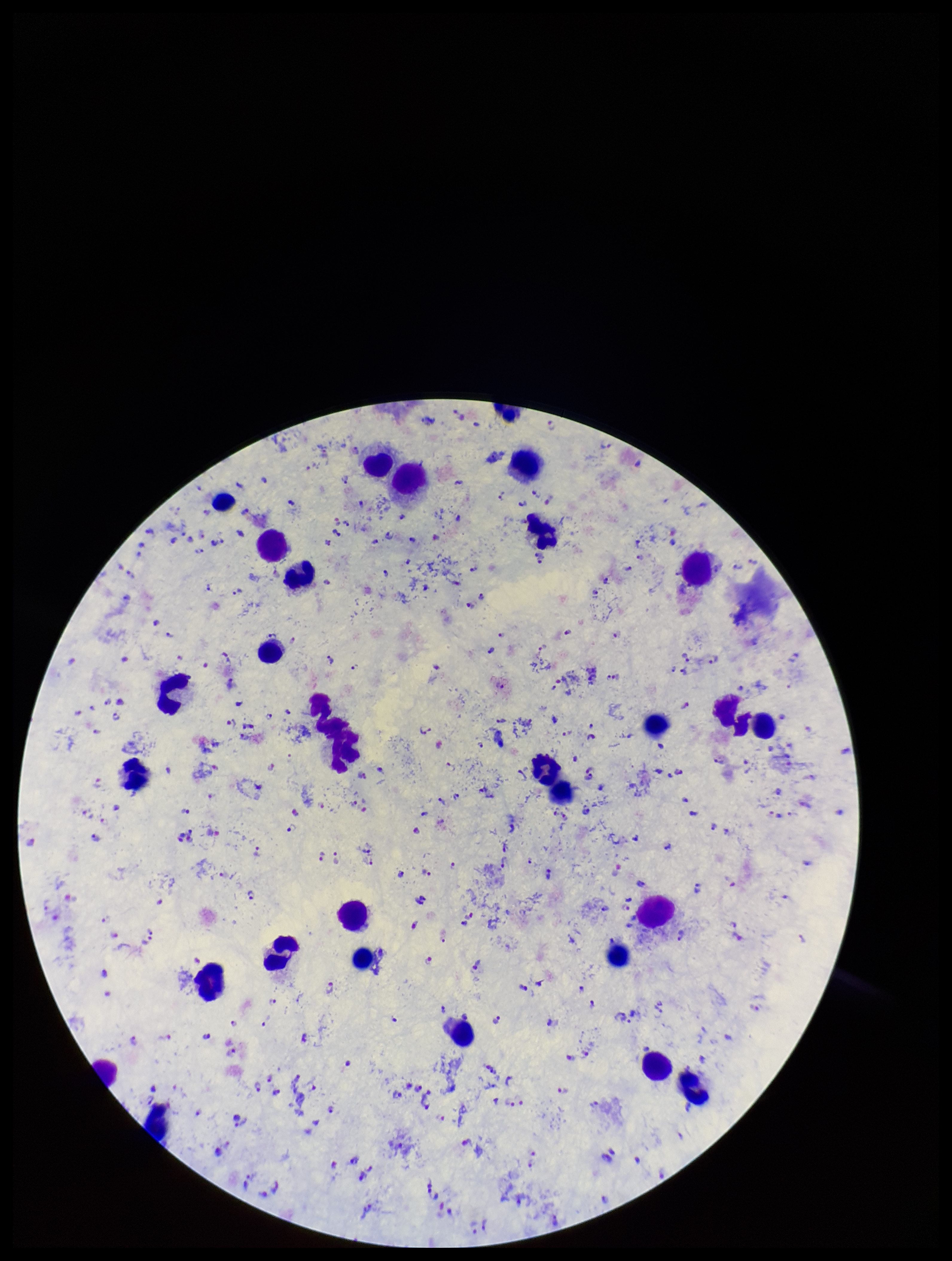

Giemsa stain. Patient malaria status: positive. Leukocyte count: 30. Species reported for this patient: Plasmodium falciparum. Plasmodium parasites: identified. Photographed through the microscope eyepiece with a smartphone camera. Preparation: thick smear. Image is 952×1261 pixels. Parasite count: 247. One field from this slide.